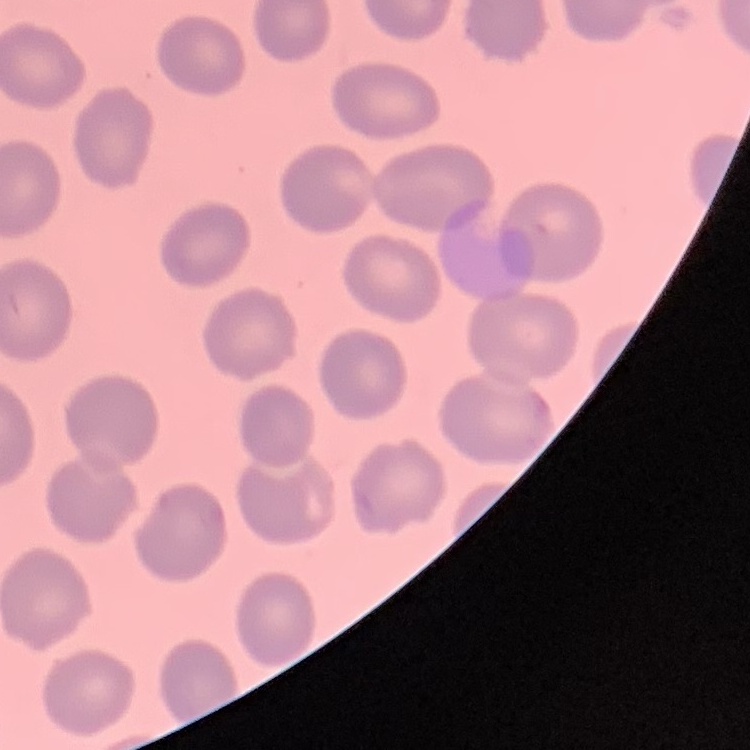
red_blood_cell_morphology: no rouleaux formation
stain: Field's or Giemsa
image_type: square crop of a larger photomicrograph
preparation: thin peripheral smear